Report the malaria status of this cell.
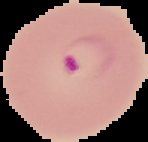
It is parasitized.

Summary:
  - Image size: 148×142 pixels
  - Preparation: thin blood film
  - Image type: segmented cell region on a black background